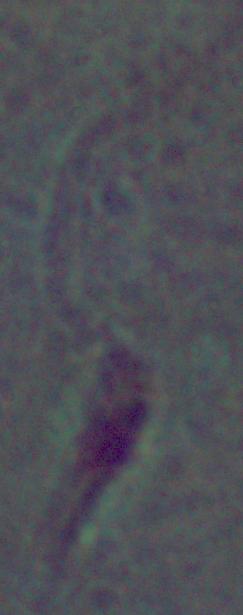

A Leishmania parasite is shown. Captured at 1000x magnification. Photomicrograph.